Report the malaria status of this cell.
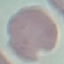

Uninfected.

Summary:
  - Stain: Giemsa
  - Image type: cell patch, automatically extracted from a larger field of view and resized to 64 × 64 pixels
  - Preparation: thin blood film
  - Capture: smartphone through the microscope eyepiece